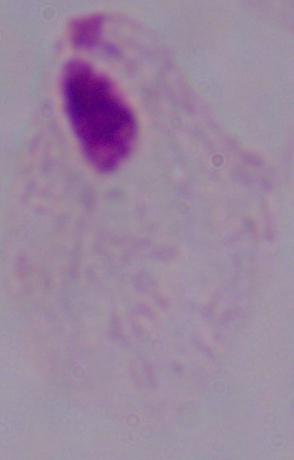

identification: trichomonad
modality: photomicrograph
magnification: 1000x